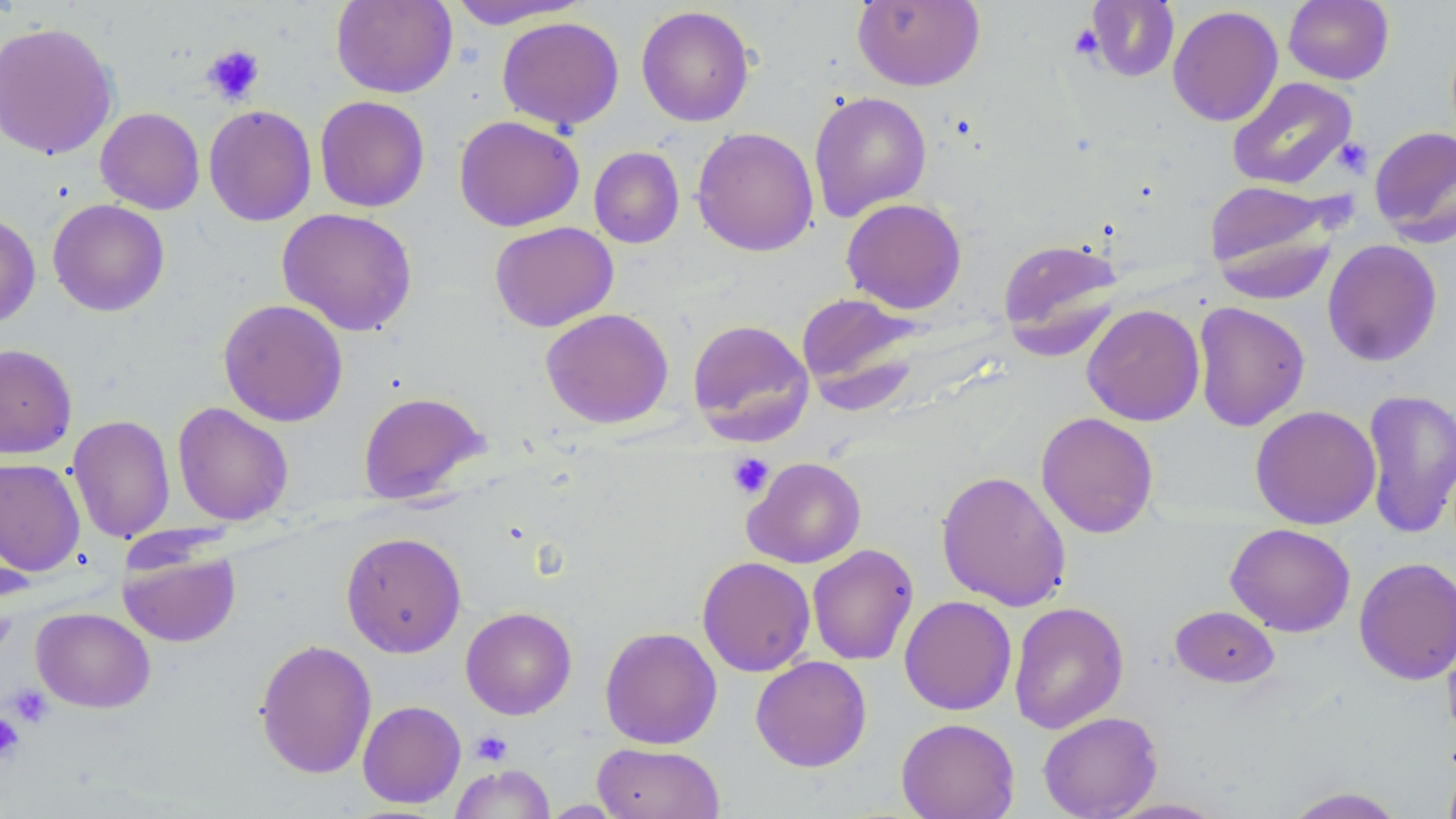
slide-level diagnosis = negative for blood parasites
stain = May-Grünwald-Giemsa
field of view = single
preparation = thin blood film
magnification = 1000x
modality = optical microscopy
uninfected red blood cell locations = approximate bounding boxes as [x1, y1, x2, y2] in pixels: [330, 0, 457, 98], [446, 0, 591, 29], [852, 0, 984, 90], [1084, 0, 1180, 82], [1283, 0, 1394, 85], [636, 5, 755, 127], [1168, 5, 1283, 127], [497, 16, 624, 131], [0, 20, 119, 160], [1227, 76, 1357, 190], [808, 91, 932, 221], [314, 95, 430, 212], [203, 104, 317, 226], [95, 107, 205, 215], [454, 115, 584, 231], [1369, 125, 1456, 246], [691, 126, 819, 256], [589, 146, 684, 248], [1205, 179, 1341, 297], [47, 198, 170, 316], [841, 198, 967, 314], [276, 207, 418, 336], [0, 212, 41, 327], [490, 221, 618, 332], [997, 236, 1125, 357], [1322, 238, 1442, 367], [796, 291, 925, 410], [217, 299, 349, 427], [1193, 301, 1310, 432], [1081, 304, 1205, 426], [541, 308, 673, 428], [687, 319, 814, 444], [0, 343, 77, 459], [1362, 389, 1456, 539], [357, 391, 489, 505], [172, 402, 294, 526], [1250, 405, 1381, 529], [1035, 412, 1159, 538], [67, 414, 176, 543], [743, 456, 866, 568], [0, 457, 85, 577], [935, 469, 1072, 612], [1226, 523, 1356, 637], [341, 531, 467, 657], [807, 543, 919, 665], [118, 545, 241, 647], [697, 556, 815, 676], [1354, 556, 1456, 686], [899, 595, 1017, 715], [1009, 601, 1129, 733], [1169, 605, 1279, 688], [460, 606, 577, 719], [32, 607, 155, 713], [599, 626, 722, 749], [1442, 628, 1456, 749], [254, 638, 377, 779], [750, 655, 872, 772], [357, 700, 466, 808], [1037, 711, 1163, 819], [896, 717, 1020, 819], [592, 742, 725, 819], [1441, 754, 1456, 819], [449, 763, 556, 819], [1280, 787, 1407, 818], [1101, 797, 1229, 818], [540, 800, 627, 817]
platelet locations = approximate bounding boxes as [x1, y1, x2, y2] in pixels: [1068, 24, 1105, 60], [201, 44, 266, 106], [1332, 137, 1373, 178], [728, 452, 775, 499], [6, 683, 51, 728], [0, 711, 24, 762], [471, 730, 513, 766]
image size = 1456×819 pixels